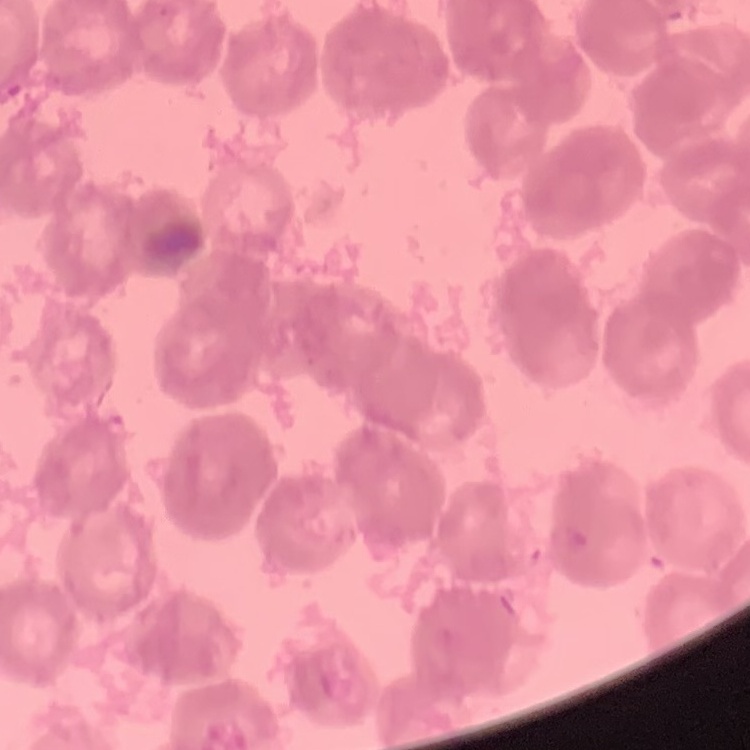 The erythrocytes show rouleaux formation. Square crop of a larger photomicrograph. Field's or Giemsa stain. Thin peripheral smear.